Locate every Plasmodium parasite.
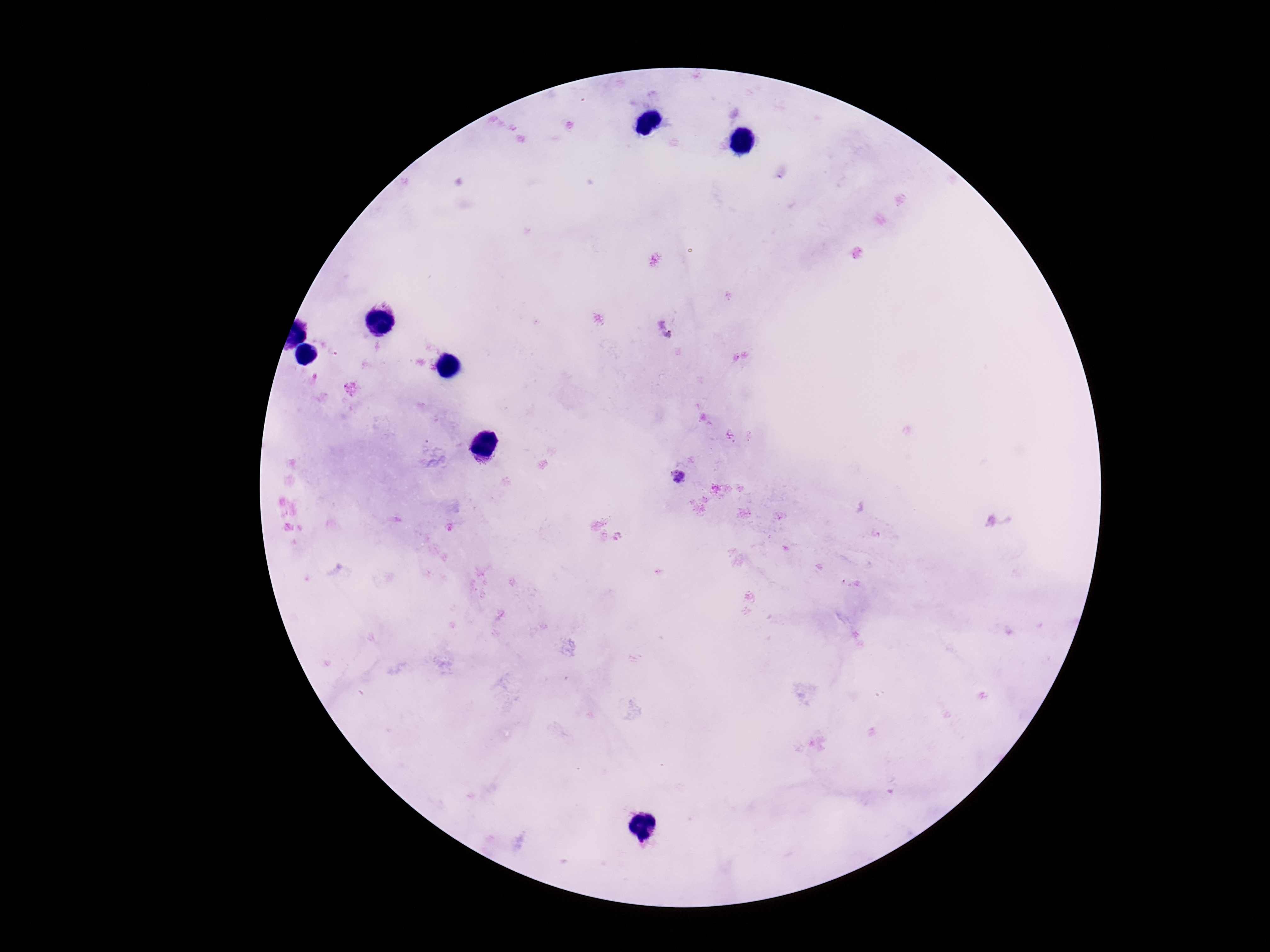
Approximate centers as {x, y} in pixels.
Plasmodium parasites: {680, 477}.

Summary:
  - Preparation: thick blood film
  - Stain: Giemsa
  - Field of view: single
  - Patient malaria status: infected
  - Capture: smartphone camera through the microscope eyepiece
  - Magnification: 100x
  - Image size: 1270×952 pixels